Locate every blood parasite and identify its species.
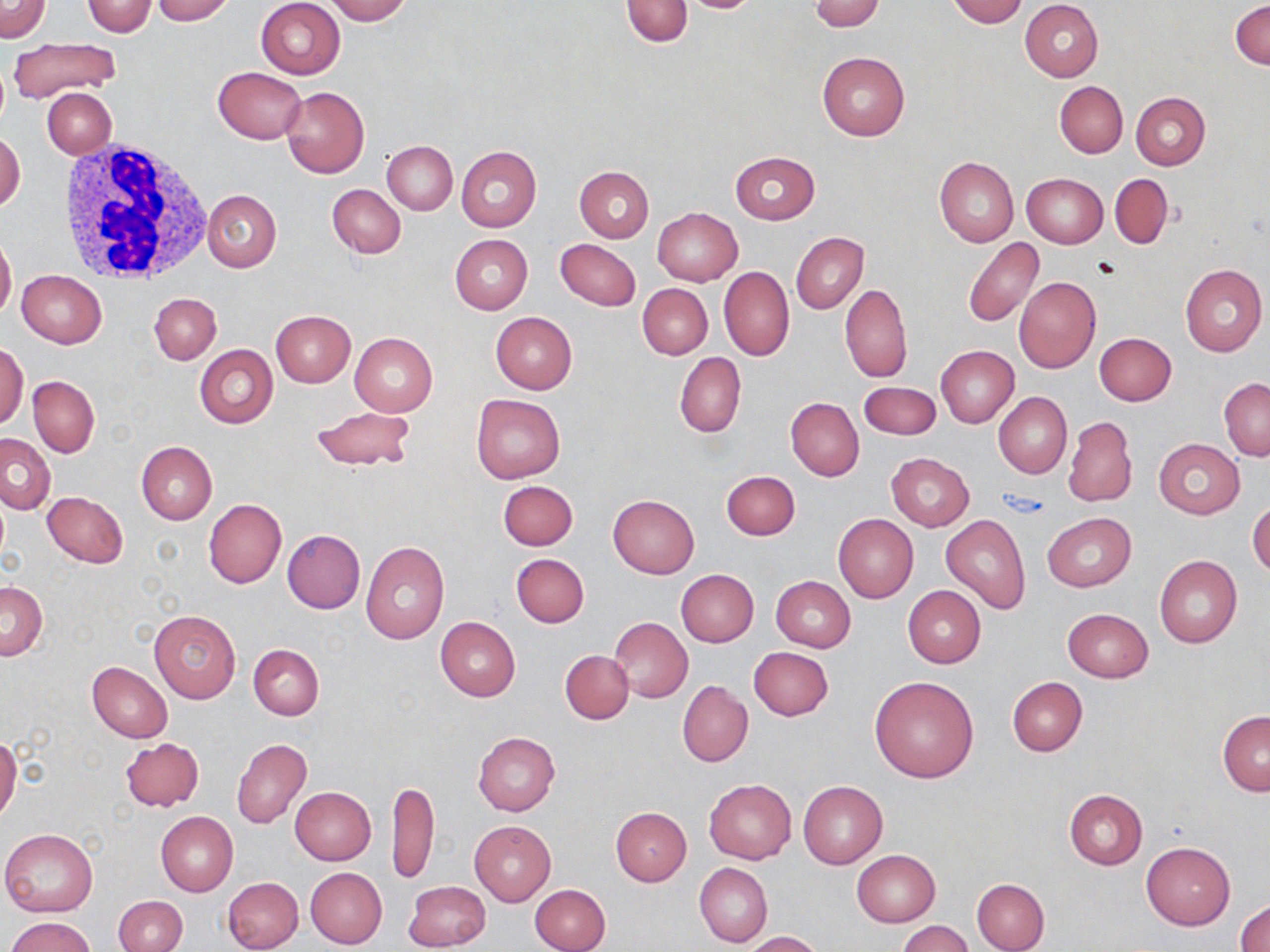

No blood parasites observed.

Summary:
  - Coordinate format: approximate bounding boxes as [x1, y1, x2, y2] in pixels
  - Uninfected red blood cell locations: [0, 0, 50, 43], [152, 0, 234, 24], [255, 0, 346, 79], [325, 0, 411, 24], [620, 0, 692, 45], [676, 0, 765, 14], [810, 0, 884, 32], [948, 0, 1025, 26], [82, 1, 157, 36], [1020, 1, 1103, 81], [1231, 1, 1269, 69], [8, 36, 123, 105], [816, 52, 909, 142], [213, 66, 306, 143], [1055, 81, 1127, 158], [280, 85, 370, 178], [43, 88, 116, 158], [1131, 92, 1210, 170], [1, 131, 25, 212], [383, 141, 457, 215], [456, 146, 541, 232], [729, 151, 819, 225], [934, 156, 1019, 247], [574, 165, 654, 242], [1110, 173, 1172, 248], [1023, 174, 1108, 248], [328, 184, 406, 258], [202, 189, 281, 271], [652, 208, 743, 286], [791, 232, 868, 314], [0, 235, 16, 318], [449, 235, 532, 315], [962, 238, 1044, 327], [555, 239, 641, 311], [1180, 265, 1267, 357], [719, 268, 794, 361], [16, 271, 107, 348], [1013, 275, 1101, 373], [638, 283, 712, 358], [839, 284, 912, 383], [150, 294, 221, 364], [270, 310, 355, 387], [491, 312, 577, 393], [349, 333, 437, 416], [1094, 333, 1176, 405], [0, 343, 28, 430], [194, 345, 278, 429], [936, 345, 1019, 427], [674, 352, 746, 437], [29, 375, 99, 457], [1219, 376, 1269, 460], [858, 381, 941, 439], [994, 392, 1072, 478], [471, 394, 566, 483], [785, 398, 864, 481], [309, 406, 415, 471], [1063, 416, 1137, 508], [0, 433, 55, 514], [1153, 439, 1245, 519], [137, 441, 217, 524], [887, 453, 974, 531], [721, 471, 799, 539], [498, 480, 578, 551], [41, 490, 128, 569], [608, 495, 699, 578], [203, 499, 286, 588], [1247, 499, 1270, 579], [1042, 513, 1136, 591], [833, 514, 918, 603], [941, 515, 1031, 614], [281, 529, 365, 614], [361, 541, 449, 644], [512, 553, 589, 628], [1154, 555, 1242, 648], [676, 569, 759, 646], [771, 576, 856, 652], [0, 582, 47, 660], [902, 585, 986, 668], [1063, 608, 1152, 682], [148, 609, 241, 703], [435, 617, 521, 701], [609, 617, 692, 703], [249, 643, 323, 720], [749, 646, 833, 721], [561, 649, 633, 724], [87, 661, 173, 743], [870, 675, 979, 782], [1007, 676, 1086, 756], [678, 681, 753, 767], [1217, 711, 1270, 797], [473, 732, 560, 816], [0, 735, 22, 822], [120, 737, 204, 812], [232, 737, 312, 828], [704, 778, 796, 864], [387, 779, 439, 886], [798, 781, 888, 868], [290, 786, 376, 864], [301, 787, 380, 946], [1064, 789, 1147, 869], [611, 807, 691, 886], [155, 811, 238, 896], [469, 820, 555, 906], [1, 829, 97, 916], [1141, 843, 1234, 929], [851, 849, 939, 927], [695, 863, 772, 947], [305, 867, 386, 948], [222, 876, 303, 952], [971, 878, 1049, 952], [405, 881, 490, 950], [530, 883, 611, 952], [114, 896, 186, 952], [1235, 899, 1270, 952], [7, 917, 97, 952], [896, 920, 971, 952], [743, 931, 825, 952]
  - White blood cell locations: [58, 142, 212, 285]
  - Slide-level diagnosis: negative for blood parasites
  - Image size: 1270×952 pixels
  - Field of view: single
  - Modality: light microscopy
  - Magnification: 1000x
  - Preparation: thin blood film
  - Stain: May-Grünwald-Giemsa